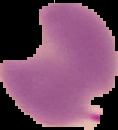
Summary:
  - Image type: segmented cell region on a black background
  - Preparation: thin blood film
  - Image size: 118×130 pixels
  - Result: malaria parasites detected